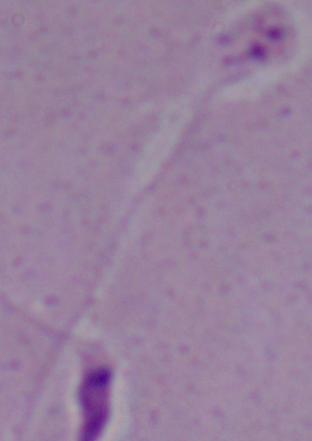

Photomicrograph. A Leishmania parasite is seen. 1000x magnification.